Locate and identify every blood parasite.
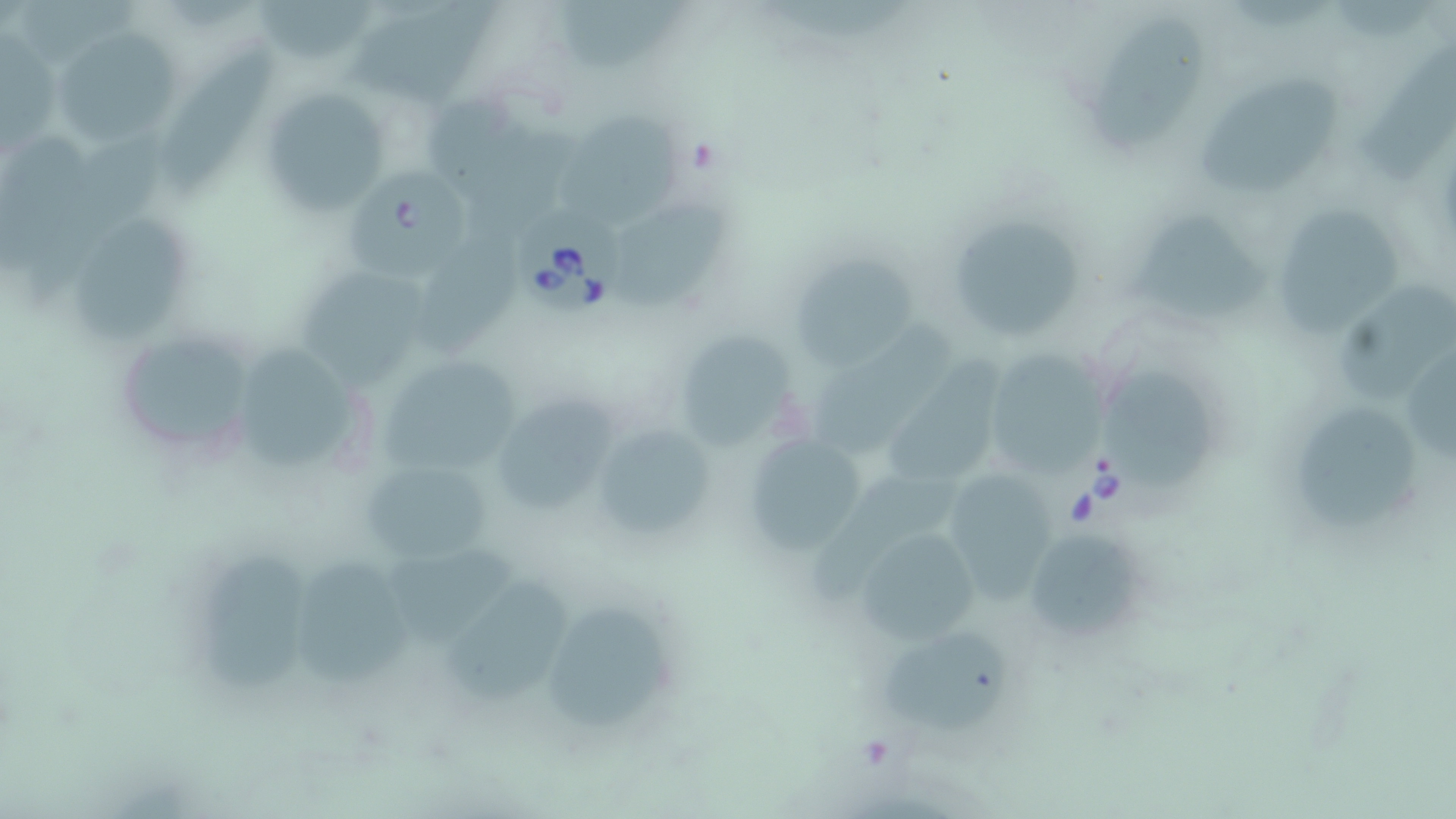

Approximate bounding boxes as [x1, y1, x2, y2] in pixels.
Babesia divergens-infected red blood cells: [349, 167, 475, 286], [514, 202, 629, 321].
No Plasmodium falciparum, Plasmodium ovale, Plasmodium malariae, Plasmodium vivax, or Trypanosoma brucei observed.

Summary:
  - Uninfected red blood cell locations: [258, 0, 378, 65], [558, 0, 685, 75], [343, 1, 497, 106], [1086, 20, 1206, 150], [53, 28, 183, 151], [1358, 44, 1456, 189], [160, 45, 282, 192], [1194, 75, 1347, 195], [258, 85, 394, 218], [430, 94, 579, 221], [559, 111, 691, 227], [619, 204, 731, 311], [941, 204, 1089, 343], [1275, 206, 1403, 340], [1121, 211, 1271, 321], [77, 213, 201, 340], [419, 228, 526, 361], [794, 251, 920, 367], [298, 277, 429, 390], [1332, 284, 1454, 406], [815, 320, 953, 447], [111, 327, 263, 462], [669, 329, 806, 454], [1407, 346, 1456, 462], [248, 347, 356, 472], [981, 347, 1112, 488], [377, 351, 530, 485], [1100, 364, 1211, 487], [881, 377, 995, 494], [489, 392, 623, 524], [1298, 404, 1418, 534], [590, 422, 717, 546], [740, 432, 869, 557], [358, 457, 493, 567], [811, 475, 959, 603], [949, 477, 1063, 604], [850, 523, 987, 647], [1021, 525, 1147, 646], [389, 549, 514, 647], [199, 555, 314, 690], [296, 560, 416, 688], [445, 577, 570, 704], [549, 604, 672, 734], [878, 630, 1009, 729]
  - Slide-level diagnosis: Babesia divergens
  - Magnification: 1000x
  - Field of view: single
  - Image size: 1456×819 pixels
  - Stain: May-Grünwald-Giemsa
  - Preparation: thin blood film
  - Modality: optical microscopy